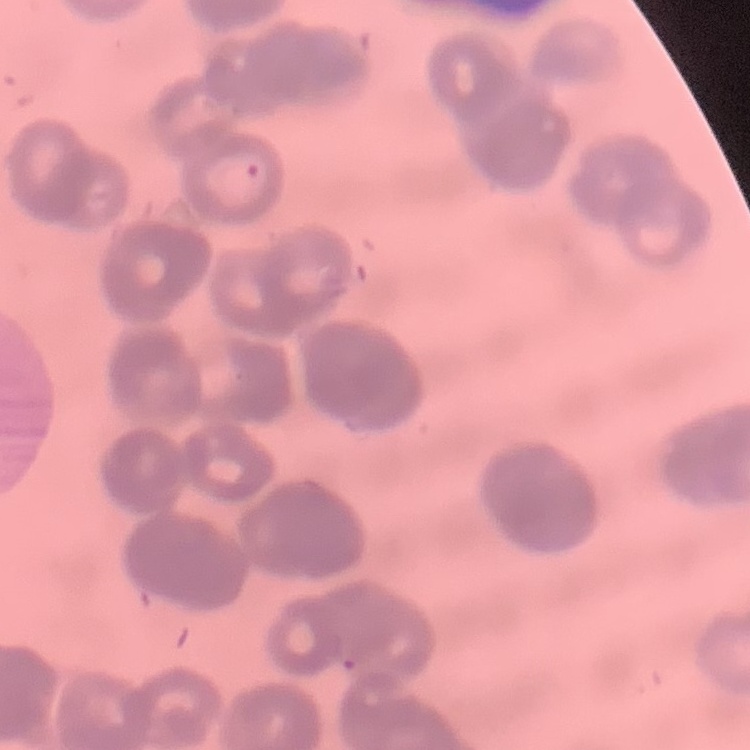
The red blood cells exhibit rouleaux formation. Thin blood smear. Stained with either Field's or Giemsa. One tile cut from a larger photomicrograph.